Give the extent of the Plasmodium malariae parasites you find, grouped by life-cycle stage — ring form, trophozoite, schizont, or gametocyte.
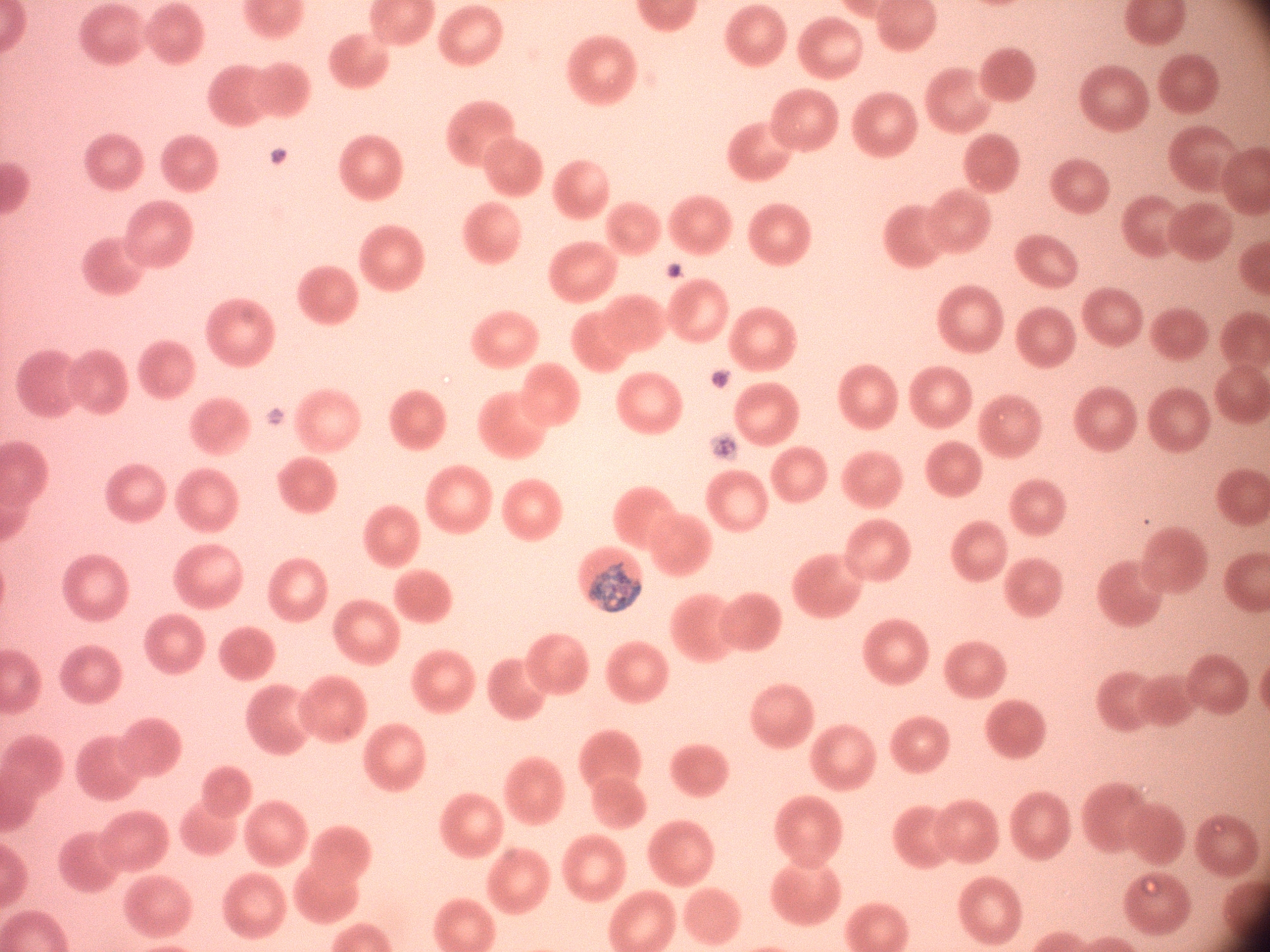

Approximate bounding boxes as (x1,y1)-(x2,y2) corner pairs in pixels, from the source annotation, which is not necessarily exhaustive.
Schizonts: (589,561)-(641,613).

{
  "preparation": "thin blood film",
  "image_size": "1270×952 pixels",
  "stain": "Giemsa",
  "species": "Plasmodium malariae",
  "magnification": "100x",
  "microscope": "Leica DM2000 with built-in camera",
  "field_of_view": "one from this slide"
}